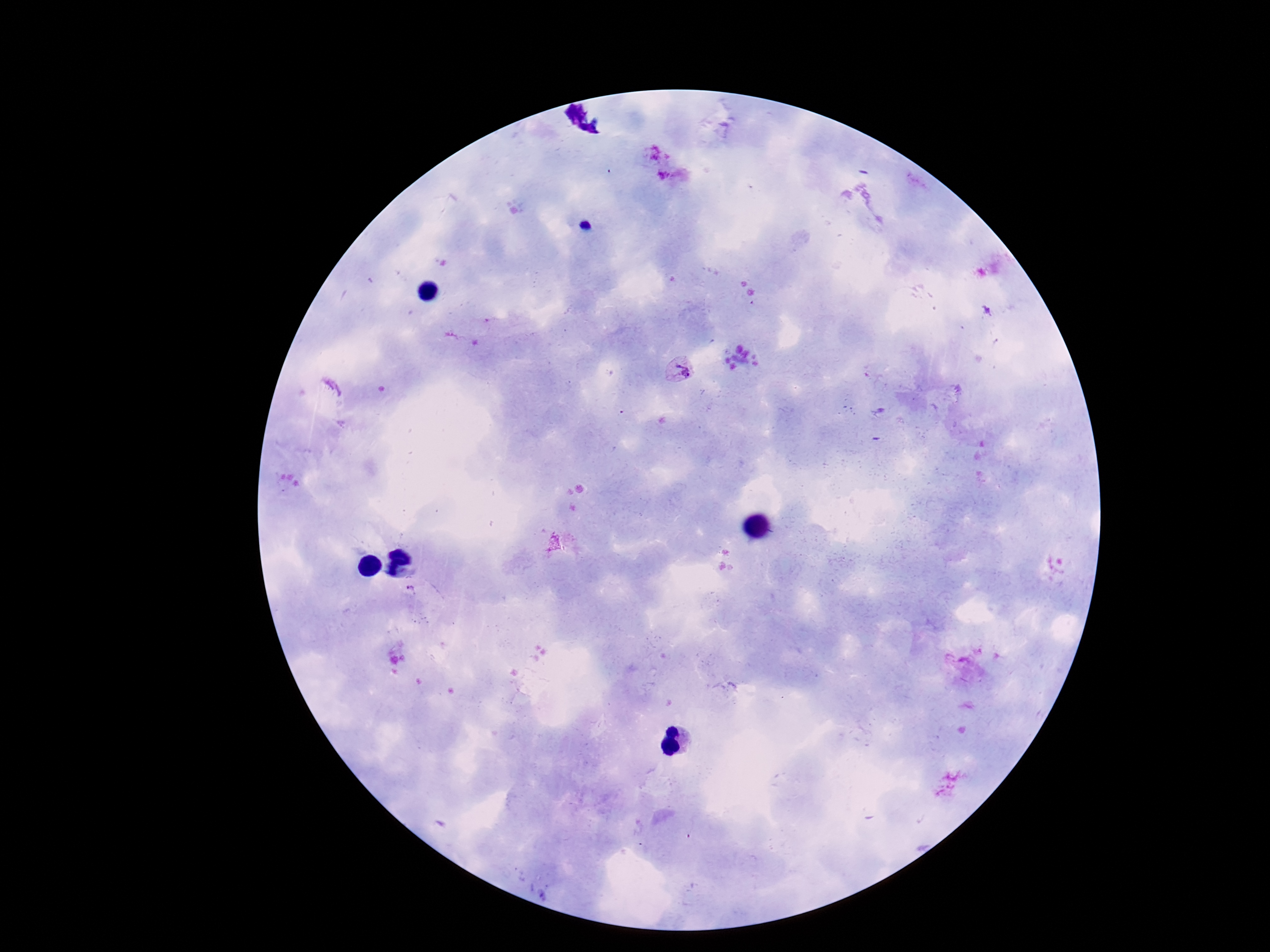
Approximate object centers, in pixels from the top-left corner.
Summary:
  - Plasmodium parasite locations: (x=655, y=154), (x=673, y=182), (x=679, y=371), (x=413, y=593)
  - Stain: Giemsa
  - Preparation: thick blood film
  - Patient malaria status: positive
  - Magnification: 100x
  - Field of view: single
  - Image size: 1270×952 pixels
  - Capture: smartphone camera through the microscope eyepiece